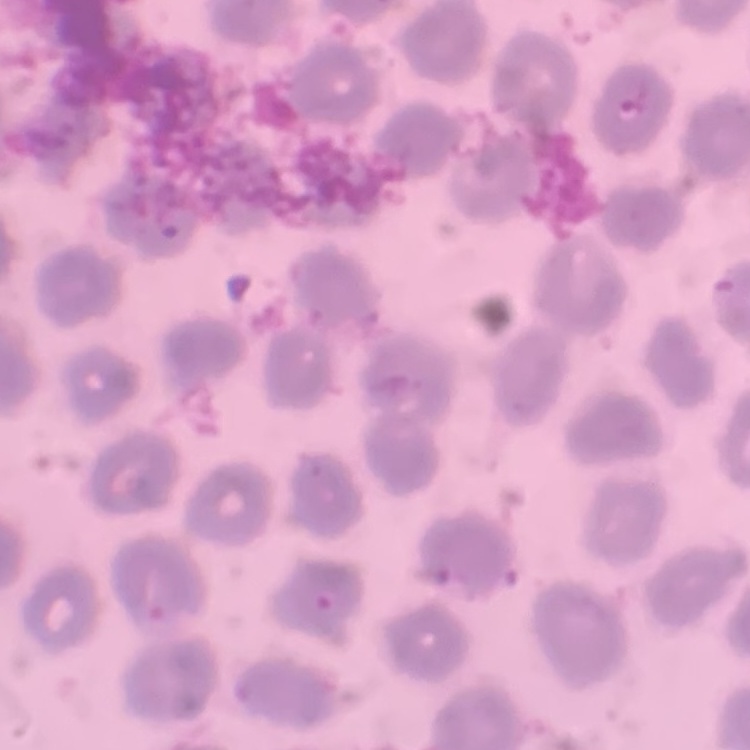
The red blood cells show no rouleaux formation. Field's or Giemsa stain. Thin blood smear. One tile cut from a larger photomicrograph.